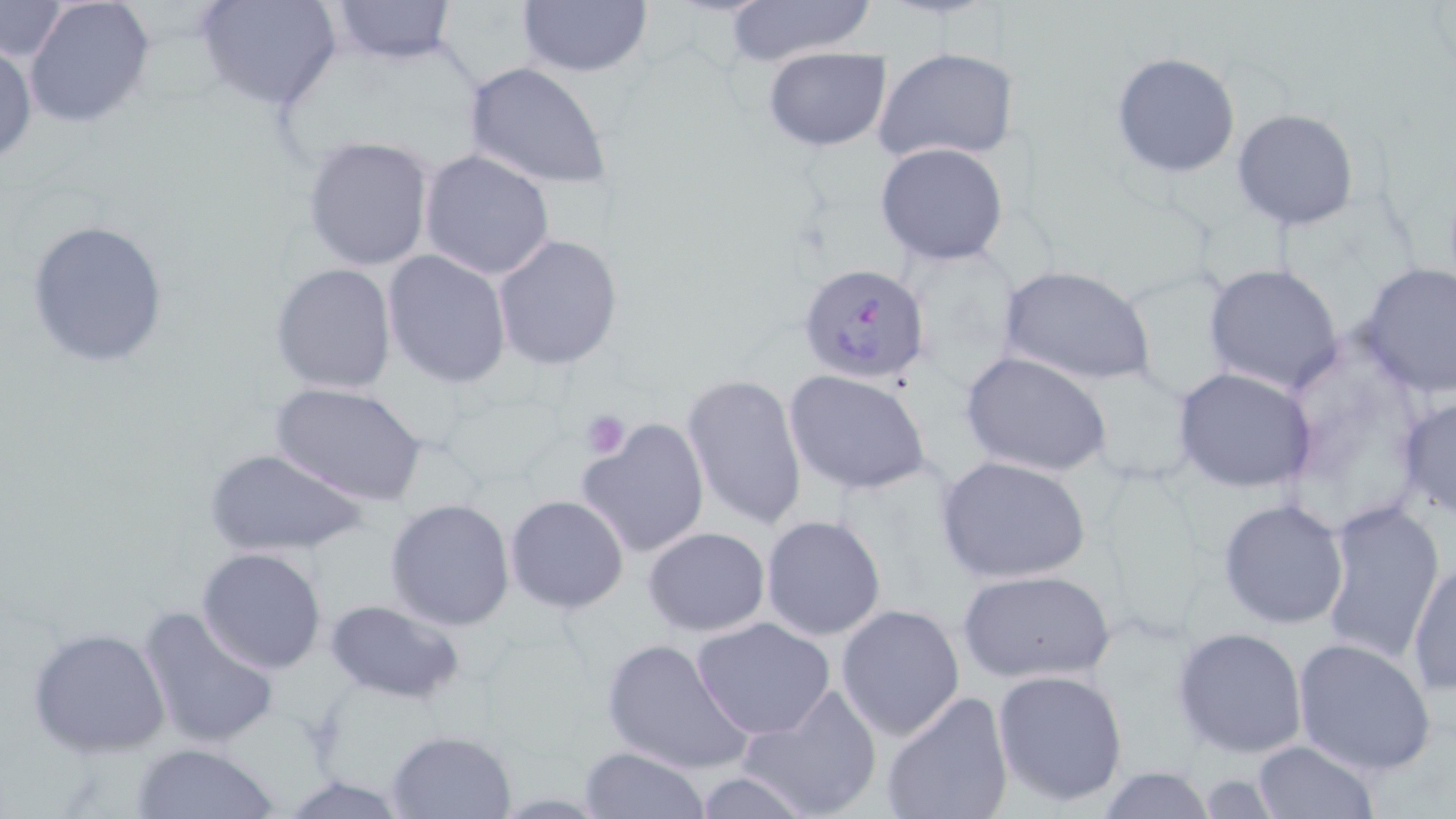

Summary:
  - Coordinate format: approximate bounding boxes as named x1/y1/x2/y2 corners in pixels
  - Uninfected red blood cell locations: (x1=24, y1=0, x2=156, y2=129), (x1=198, y1=0, x2=340, y2=110), (x1=516, y1=0, x2=652, y2=76), (x1=718, y1=0, x2=879, y2=66), (x1=330, y1=1, x2=456, y2=65), (x1=0, y1=3, x2=71, y2=61), (x1=1, y1=42, x2=37, y2=166), (x1=762, y1=46, x2=891, y2=149), (x1=873, y1=46, x2=1021, y2=167), (x1=1112, y1=53, x2=1241, y2=177), (x1=462, y1=61, x2=613, y2=191), (x1=1232, y1=108, x2=1360, y2=231), (x1=302, y1=134, x2=435, y2=272), (x1=876, y1=142, x2=1010, y2=266), (x1=419, y1=150, x2=555, y2=281), (x1=24, y1=218, x2=170, y2=368), (x1=492, y1=235, x2=624, y2=371), (x1=383, y1=251, x2=512, y2=388), (x1=1355, y1=262, x2=1456, y2=397), (x1=270, y1=263, x2=397, y2=394), (x1=1203, y1=263, x2=1348, y2=395), (x1=999, y1=267, x2=1153, y2=386), (x1=961, y1=352, x2=1111, y2=478), (x1=1172, y1=366, x2=1318, y2=493), (x1=786, y1=371, x2=930, y2=495), (x1=681, y1=373, x2=807, y2=530), (x1=271, y1=381, x2=429, y2=506), (x1=1399, y1=394, x2=1456, y2=522), (x1=578, y1=417, x2=711, y2=561), (x1=204, y1=448, x2=371, y2=558), (x1=935, y1=454, x2=1092, y2=584), (x1=503, y1=495, x2=629, y2=613), (x1=385, y1=497, x2=514, y2=632), (x1=1218, y1=499, x2=1351, y2=629), (x1=1316, y1=499, x2=1443, y2=667), (x1=760, y1=515, x2=887, y2=642), (x1=643, y1=527, x2=769, y2=636), (x1=196, y1=547, x2=327, y2=675), (x1=1407, y1=560, x2=1455, y2=699), (x1=955, y1=569, x2=1116, y2=683), (x1=324, y1=598, x2=464, y2=704), (x1=138, y1=604, x2=280, y2=750), (x1=835, y1=604, x2=965, y2=741), (x1=691, y1=617, x2=838, y2=739), (x1=28, y1=626, x2=170, y2=757), (x1=1173, y1=626, x2=1309, y2=758), (x1=600, y1=636, x2=755, y2=775), (x1=1292, y1=636, x2=1437, y2=775), (x1=993, y1=669, x2=1128, y2=807), (x1=736, y1=684, x2=883, y2=819), (x1=879, y1=690, x2=1015, y2=819), (x1=386, y1=730, x2=515, y2=818), (x1=1249, y1=740, x2=1381, y2=819), (x1=128, y1=742, x2=283, y2=818), (x1=579, y1=746, x2=707, y2=818), (x1=1094, y1=767, x2=1219, y2=818), (x1=279, y1=774, x2=414, y2=817)
  - Platelet locations: (x1=581, y1=409, x2=630, y2=455)
  - Plasmodium falciparum-infected red blood cell locations: (x1=799, y1=265, x2=931, y2=383)
  - Slide-level diagnosis: Plasmodium falciparum
  - Magnification: 1000x
  - Preparation: thin blood smear
  - Image size: 1456×819 pixels
  - Stain: May-Grünwald-Giemsa
  - Field of view: single
  - Modality: optical microscopy